Comment on the morphology of the red blood cells.
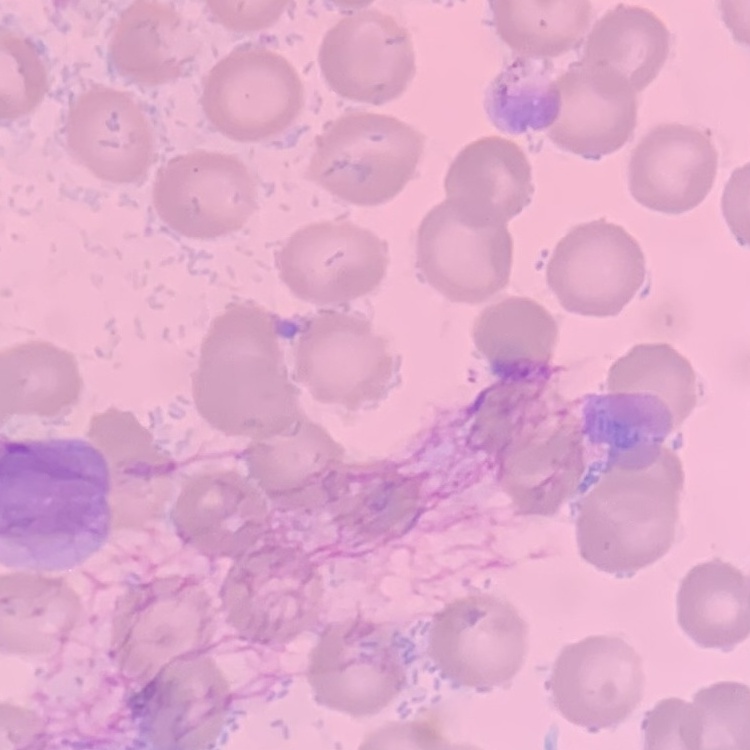
They show no rouleaux formation.

image_type: square crop of a larger photomicrograph
preparation: thin blood film
stain: Field's or Giemsa